Locate every Plasmodium parasite and every leukocyte.
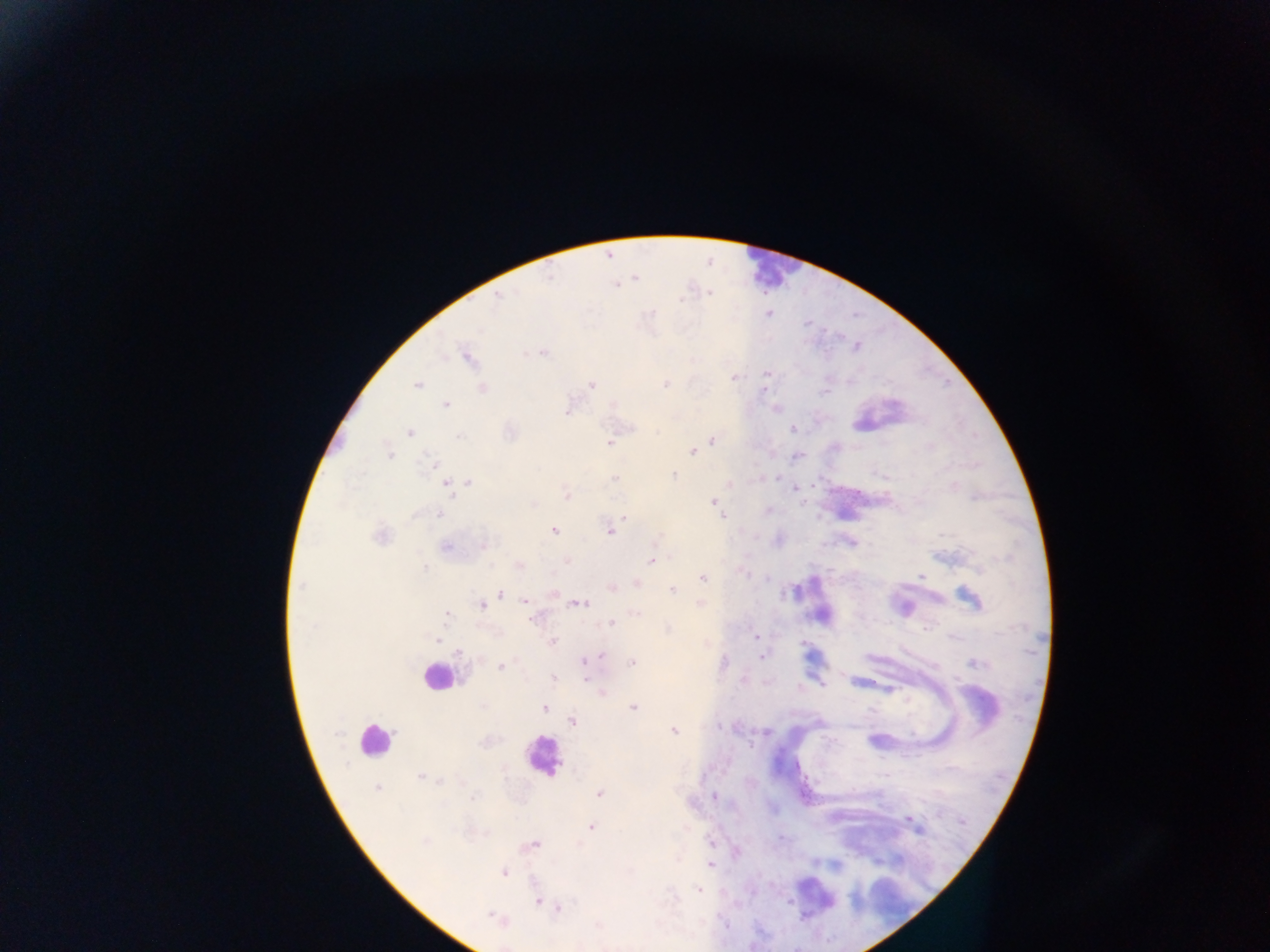
Approximate centers as {x, y} in pixels.
Plasmodium parasites: {549, 277}, {635, 278}, {616, 285}, {709, 292}, {498, 295}, {681, 300}, {768, 313}, {856, 346}, {543, 353}, {468, 357}, {766, 373}, {734, 378}, {417, 384}, {665, 384}, {591, 385}, {482, 388}, {764, 391}, {447, 405}, {567, 412}, {791, 428}, {410, 432}, {460, 435}, {712, 440}, {609, 443}, {692, 451}, {389, 452}, {432, 463}, {674, 475}, {616, 477}, {462, 484}, {451, 486}, {567, 495}, {713, 502}, {720, 512}, {440, 514}, {624, 516}, {723, 517}, {554, 531}, {610, 531}, {380, 537}, {485, 545}, {446, 547}, {651, 561}, {920, 576}, {702, 578}, {672, 590}, {501, 594}, {524, 601}, {580, 603}, {700, 604}, {482, 605}, {446, 615}, {532, 618}, {610, 623}, {756, 636}, {437, 640}, {553, 642}, {601, 656}, {761, 656}, {584, 661}, {632, 663}, {975, 663}, {501, 667}, {553, 678}, {586, 679}, {601, 692}, {544, 707}, {633, 707}, {573, 722}, {674, 731}, {421, 777}, {377, 788}, {600, 794}, {713, 796}, {590, 827}, {424, 841}, {534, 844}, {711, 864}, {504, 872}, {699, 890}, {538, 903}, {559, 908}, {493, 917}.
Leukocytes: {773, 270}, {436, 676}, {373, 741}, {542, 756}.

Summary:
  - Country: Ghana
  - Image size: 1270×952 pixels
  - Field of view: single
  - Capture: mobile-phone photograph through a microscope
  - Preparation: thick blood smear